Give the preparation type.
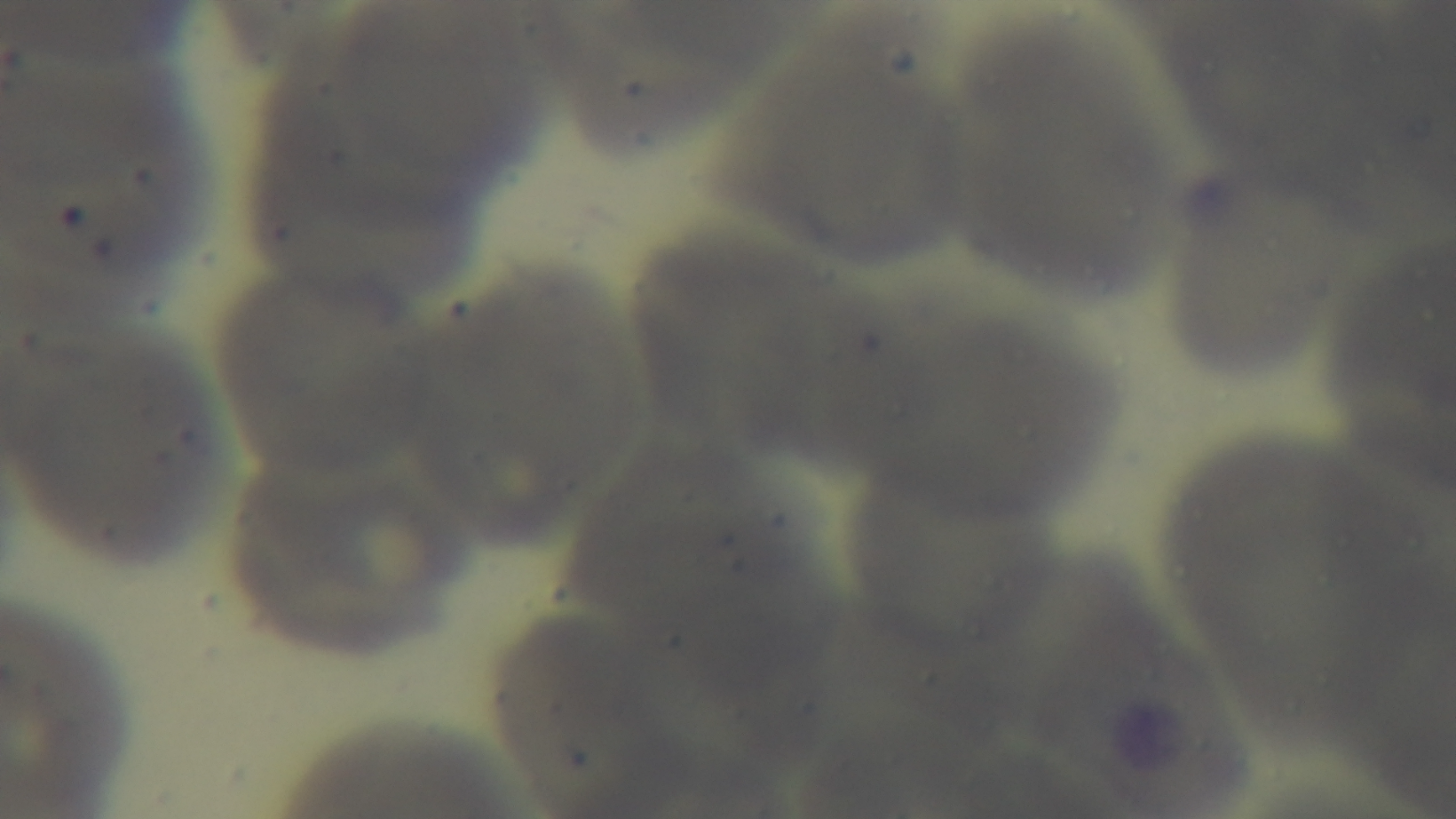
It is a thin blood film.

Summary:
  - Field of view: one from the slide
  - Modality: light microscopy
  - Capture: mounted 4K digital camera
  - Objective: 100x oil immersion
  - Malaria status: negative
  - Stain: Giemsa